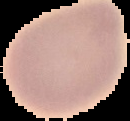
preparation = thin blood smear
image type = segmented cell region on a black background
malaria status = uninfected
image size = 130×121 pixels